Identify the parasite.
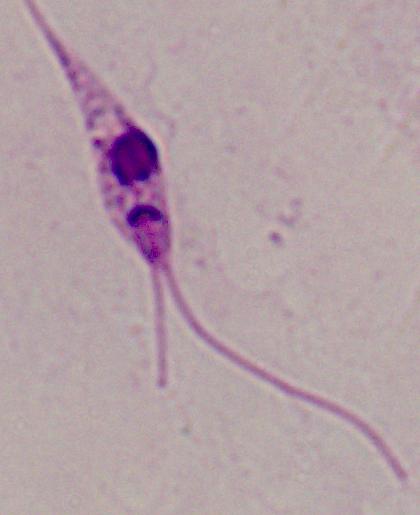

This is Leishmania.

Summary:
  - Modality: micrograph
  - Magnification: 1000x